Outline each blood parasite and name the species.
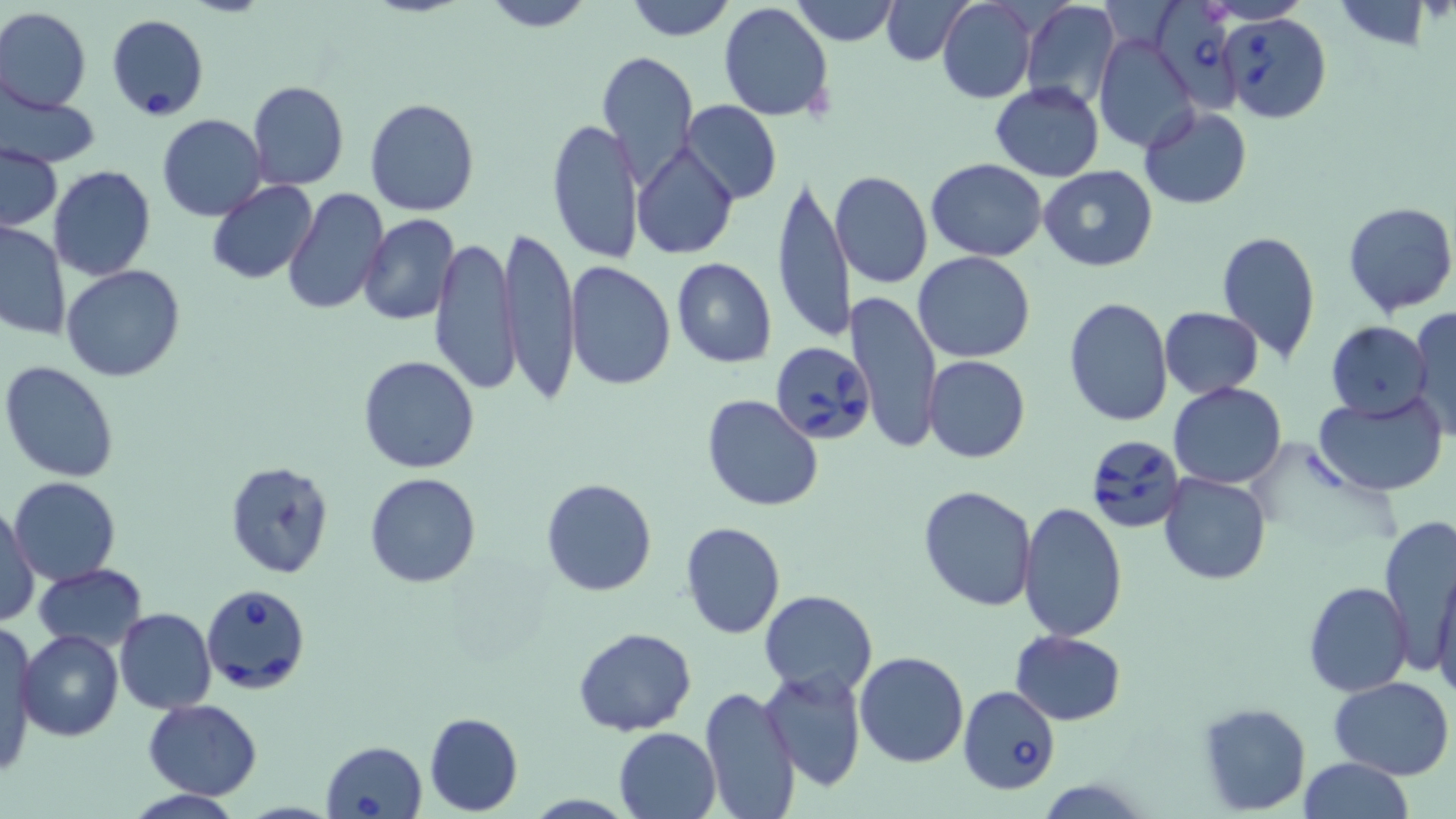
Approximate bounding boxes as [x1, y1, x2, y2] in pixels.
Babesia divergens-infected red blood cells: [1153, 0, 1248, 121], [1221, 12, 1331, 123], [106, 15, 208, 119], [770, 338, 874, 449], [1085, 433, 1187, 534], [201, 582, 311, 694], [958, 686, 1061, 796], [320, 740, 428, 818].
No Plasmodium falciparum, Plasmodium ovale, Plasmodium malariae, Plasmodium vivax, or Trypanosoma brucei observed.

Summary:
  - Uninfected red blood cell locations: [478, 0, 600, 32], [623, 0, 738, 41], [789, 0, 900, 47], [881, 0, 974, 65], [936, 0, 1036, 103], [1020, 0, 1121, 112], [1201, 0, 1315, 24], [1334, 1, 1436, 50], [718, 3, 834, 121], [0, 7, 91, 112], [1096, 33, 1201, 153], [597, 52, 699, 187], [247, 80, 348, 190], [990, 82, 1105, 181], [1, 92, 100, 168], [159, 95, 349, 203], [364, 98, 479, 218], [682, 101, 782, 204], [1139, 105, 1252, 209], [157, 114, 268, 221], [547, 115, 644, 265], [632, 144, 739, 259], [2, 146, 62, 230], [926, 158, 1048, 262], [1039, 164, 1158, 271], [49, 165, 155, 281], [831, 172, 932, 290], [773, 174, 851, 344], [208, 181, 318, 285], [282, 187, 386, 316], [1342, 202, 1456, 317], [359, 214, 460, 326], [0, 219, 71, 341], [501, 227, 580, 398], [1215, 229, 1320, 363], [430, 236, 520, 394], [914, 251, 1036, 362], [671, 258, 778, 367], [566, 260, 676, 392], [61, 265, 187, 382], [847, 288, 943, 453], [1062, 295, 1173, 427], [1406, 304, 1456, 438], [1159, 307, 1263, 398], [1326, 321, 1432, 420], [358, 355, 482, 474], [924, 355, 1030, 462], [1, 360, 120, 484], [1169, 381, 1287, 490], [1312, 392, 1448, 496], [701, 395, 823, 512], [223, 462, 332, 580], [364, 472, 482, 588], [1159, 472, 1271, 585], [9, 476, 121, 584], [541, 477, 658, 597], [917, 484, 1037, 612], [1017, 502, 1129, 642], [2, 504, 40, 627], [1377, 511, 1454, 653], [681, 521, 786, 639], [1430, 563, 1456, 701], [34, 564, 149, 651], [1303, 580, 1413, 697], [760, 589, 877, 697], [115, 607, 218, 713], [1, 626, 40, 778], [574, 627, 696, 737], [17, 629, 123, 742], [1010, 631, 1127, 725], [855, 650, 968, 767], [758, 667, 866, 793], [1329, 676, 1453, 778], [699, 685, 801, 819], [143, 699, 264, 798], [1197, 701, 1312, 816], [424, 712, 523, 814], [614, 727, 722, 819], [1299, 757, 1414, 819]
  - Slide-level diagnosis: Babesia divergens
  - Image size: 1456×819 pixels
  - Field of view: single
  - Preparation: thin blood film
  - Modality: optical microscopy
  - Stain: May-Grünwald-Giemsa
  - Magnification: 1000x